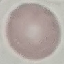 Malaria status: uninfected. Cell patch, automatically extracted from a larger field of view and resized to 64 × 64 pixels. Thin smear of blood. Giemsa stain. Acquired by smartphone through the microscope eyepiece.